Outline each Plasmodium falciparum-infected red blood cell.
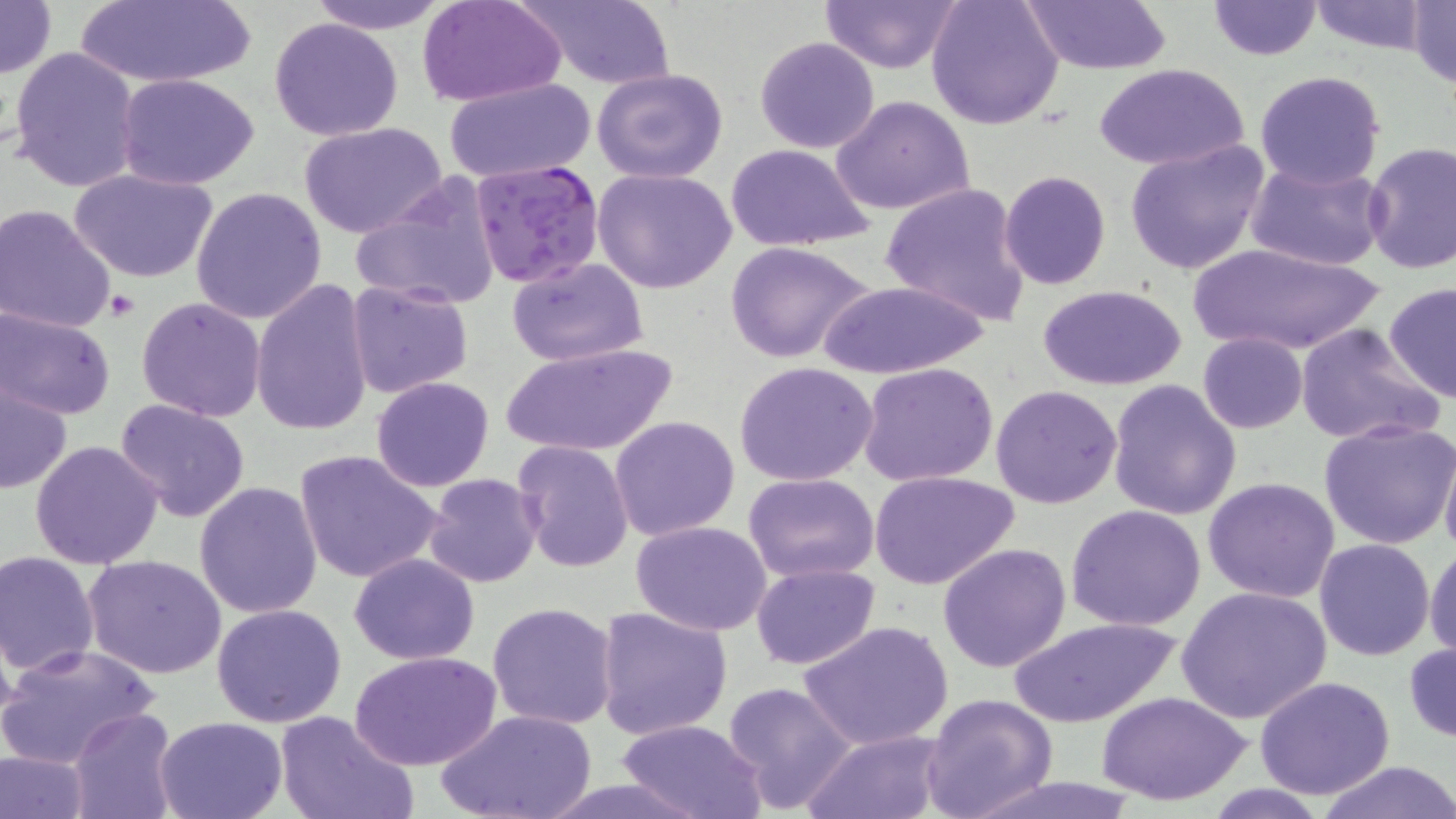
Approximate bounding boxes as [x1, y1, x2, y2] in pixels.
Plasmodium falciparum-infected red blood cells: [469, 158, 605, 290].

Summary:
  - Platelet locations: [103, 289, 141, 322]
  - Uninfected red blood cell locations: [0, 0, 55, 81], [307, 0, 452, 35], [509, 0, 676, 88], [925, 0, 1064, 130], [1019, 0, 1173, 74], [1305, 0, 1435, 54], [75, 1, 256, 88], [819, 1, 963, 72], [1206, 1, 1323, 61], [1405, 1, 1456, 87], [418, 2, 564, 106], [269, 17, 404, 141], [754, 36, 881, 154], [7, 46, 143, 194], [1094, 63, 1250, 172], [592, 67, 731, 184], [1255, 70, 1386, 189], [117, 73, 262, 188], [446, 78, 593, 184], [831, 94, 975, 218], [300, 123, 448, 239], [1124, 139, 1269, 275], [1361, 141, 1455, 275], [726, 144, 876, 251], [1246, 159, 1389, 272], [69, 166, 219, 284], [592, 168, 739, 296], [998, 171, 1111, 290], [351, 174, 504, 313], [880, 182, 1032, 329], [192, 187, 327, 324], [0, 203, 118, 333], [1181, 240, 1390, 356], [723, 241, 876, 364], [507, 257, 649, 367], [250, 279, 374, 437], [814, 279, 992, 381], [346, 281, 474, 400], [1383, 283, 1456, 403], [1035, 284, 1187, 390], [137, 296, 268, 421], [1, 307, 116, 420], [1296, 323, 1442, 447], [1196, 333, 1307, 433], [496, 342, 680, 459], [735, 361, 878, 486], [859, 361, 999, 487], [370, 376, 494, 492], [1, 377, 73, 495], [1108, 380, 1242, 523], [990, 384, 1123, 508], [114, 398, 250, 522], [610, 414, 740, 539], [1319, 417, 1456, 550], [512, 440, 633, 572], [1439, 440, 1456, 562], [29, 441, 165, 570], [293, 448, 444, 585], [870, 470, 1021, 591], [743, 472, 879, 582], [423, 473, 542, 588], [1203, 477, 1341, 604], [193, 480, 325, 620], [1065, 504, 1208, 631], [629, 520, 774, 636], [1313, 538, 1435, 660], [1424, 541, 1456, 665], [937, 543, 1072, 673], [0, 551, 101, 677], [349, 553, 480, 664], [83, 554, 228, 678], [750, 562, 879, 670], [1177, 586, 1334, 726], [486, 600, 619, 731], [211, 603, 347, 728], [594, 606, 733, 740], [1006, 615, 1180, 729], [800, 620, 954, 749], [464, 631, 610, 811], [1405, 640, 1455, 742], [0, 643, 162, 769], [351, 651, 501, 770], [1253, 676, 1397, 799], [721, 681, 858, 813], [1099, 690, 1251, 806], [919, 693, 1060, 819], [68, 708, 178, 818], [440, 709, 594, 819], [276, 710, 417, 819], [154, 716, 289, 819], [616, 719, 768, 819], [801, 730, 949, 819], [0, 748, 92, 819], [1313, 761, 1456, 819]
  - Slide-level diagnosis: Plasmodium falciparum
  - Preparation: thin blood smear
  - Field of view: one of a larger specimen
  - Modality: light microscopy
  - Stain: May-Grünwald-Giemsa
  - Image size: 1456×819 pixels
  - Magnification: 1000x